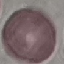

Result: no malaria parasites seen. Automatically extracted cell patch, resized to 64 × 64 pixels. Giemsa-stained preparation. Acquired by smartphone through the microscope eyepiece. Thin smear of blood.